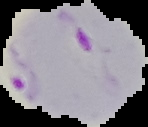
Summary:
  - Malaria status: parasitized
  - Image size: 148×127 pixels
  - Preparation: thin blood film
  - Image type: segmented cell region on a black background